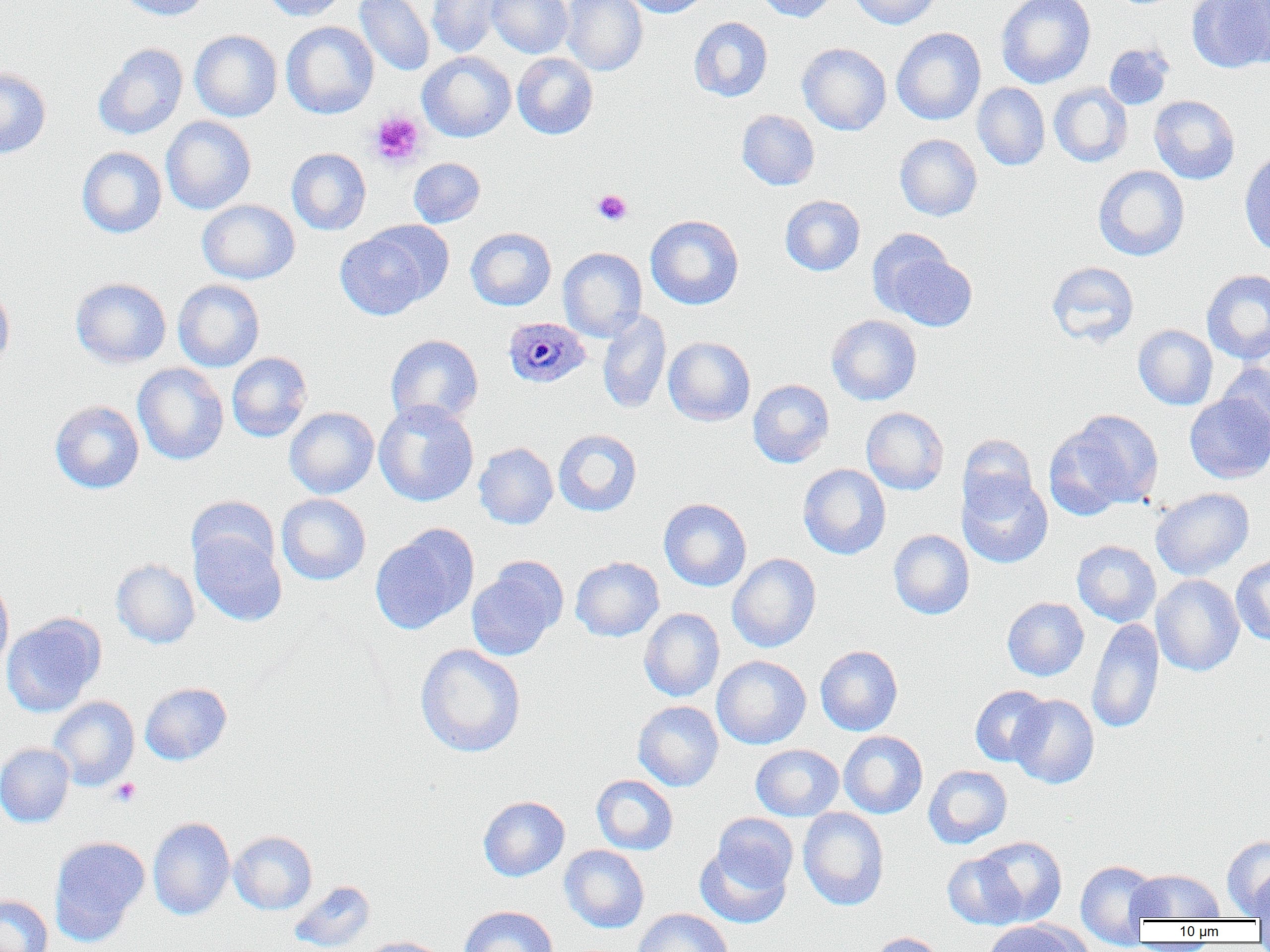
Approximate bounding boxes as [x1, y1, x2, y2] in pixels. Plasmodium ovale-infected red blood cell locations: [503, 317, 591, 389]. Platelet locations: [368, 110, 426, 168], [592, 188, 633, 226], [110, 778, 141, 807]. Uninfected red blood cell locations: [115, 0, 210, 21], [260, 0, 348, 21], [426, 0, 503, 57], [486, 0, 573, 58], [561, 0, 647, 76], [621, 0, 712, 18], [753, 0, 836, 22], [850, 0, 941, 29], [996, 0, 1096, 89], [1186, 0, 1269, 73], [354, 1, 435, 76], [1234, 2, 1270, 69], [689, 17, 773, 102], [281, 21, 379, 119], [891, 27, 986, 125], [189, 30, 282, 122], [93, 42, 188, 140], [797, 42, 891, 135], [1104, 43, 1174, 110], [418, 51, 516, 142], [513, 52, 598, 139], [0, 67, 51, 159], [1049, 82, 1133, 167], [973, 83, 1050, 171], [1149, 95, 1240, 184], [736, 109, 820, 190], [161, 116, 257, 214], [894, 134, 982, 221], [76, 146, 167, 238], [287, 148, 371, 235], [1239, 150, 1270, 257], [408, 158, 485, 228], [1093, 165, 1190, 261], [780, 195, 865, 276], [197, 199, 300, 284], [645, 214, 744, 309], [334, 226, 440, 321], [465, 227, 556, 311], [867, 228, 954, 318], [558, 247, 647, 342], [884, 250, 978, 331], [1046, 261, 1139, 347], [1201, 269, 1270, 364], [70, 277, 172, 369], [172, 279, 264, 372], [0, 280, 15, 370], [597, 310, 671, 414], [826, 314, 922, 405], [1133, 325, 1218, 409], [385, 334, 484, 427], [663, 336, 755, 426], [226, 352, 312, 442], [1218, 361, 1270, 447], [132, 362, 229, 465], [748, 379, 835, 468], [1185, 393, 1270, 483], [50, 401, 145, 494], [373, 401, 479, 506], [285, 407, 379, 499], [861, 407, 949, 495], [1048, 409, 1164, 517], [553, 428, 642, 517], [957, 434, 1038, 518], [474, 442, 558, 529], [798, 464, 891, 559], [957, 474, 1053, 569], [1151, 487, 1254, 580], [276, 494, 371, 585], [186, 496, 279, 577], [659, 498, 752, 591], [370, 525, 479, 634], [888, 529, 974, 619], [190, 530, 286, 626], [1072, 540, 1161, 626], [727, 553, 821, 652], [1231, 555, 1270, 645], [570, 556, 664, 642], [112, 558, 200, 649], [466, 559, 567, 661], [1151, 574, 1244, 676], [0, 575, 14, 675], [1002, 597, 1089, 681], [639, 608, 725, 701], [2, 613, 105, 717], [1087, 618, 1164, 734], [415, 644, 526, 757], [815, 645, 903, 736], [711, 655, 811, 749], [140, 682, 232, 765], [970, 685, 1051, 766], [1009, 694, 1099, 789], [48, 696, 139, 790], [633, 700, 723, 791], [839, 731, 928, 818], [0, 742, 74, 828], [750, 744, 844, 821], [923, 764, 1012, 849], [591, 774, 678, 855], [478, 795, 569, 881], [798, 807, 889, 910], [711, 813, 798, 893], [148, 817, 235, 920], [229, 831, 317, 914], [48, 835, 150, 945], [973, 835, 1067, 927], [1221, 835, 1270, 917], [694, 844, 792, 928], [560, 845, 649, 933], [942, 852, 1026, 930], [1076, 859, 1162, 946], [1127, 869, 1225, 921], [1248, 869, 1270, 924], [289, 881, 375, 952], [0, 895, 53, 952], [458, 905, 558, 952], [633, 908, 733, 952], [983, 920, 1088, 952], [868, 932, 948, 952], [360, 936, 450, 952]. Slide-level diagnosis: Plasmodium ovale. Thin blood film. Captured at 1000x magnification. Optical microscopy. Image is 1270×952 pixels. Single field of view.